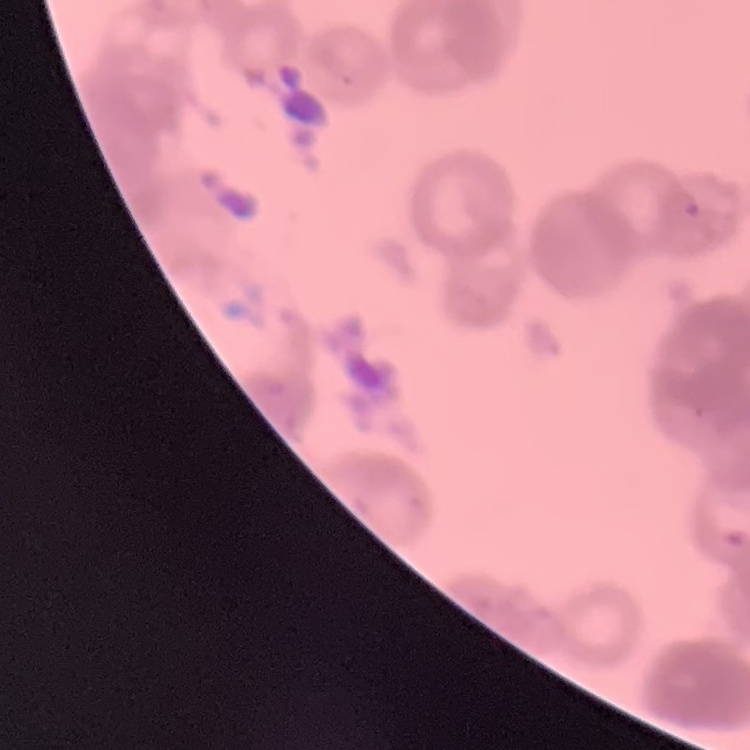

Summary:
  - Erythrocyte morphology: rouleaux formation
  - Preparation: thin blood smear
  - Stain: Field's or Giemsa
  - Image type: square crop of a larger photomicrograph